Report the malaria status of this cell.
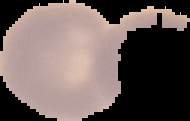
It is uninfected.

image size = 190×121 pixels
image type = cell region segmented out of the field of view; surrounding area masked to black
preparation = thin blood smear